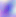
identification: Toxoplasma gondii
modality: photomicrograph
magnification: 400x